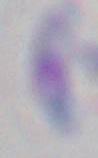

Summary:
  - Modality: micrograph
  - Identification: Toxoplasma gondii
  - Magnification: 1000x